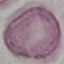
Summary:
  - Result: negative for malaria parasites
  - Preparation: thin blood smear
  - Image type: automatically extracted cell patch, resized to 64 × 64 pixels
  - Stain: Giemsa
  - Capture: smartphone through the microscope eyepiece